Locate every blood parasite and identify its species.
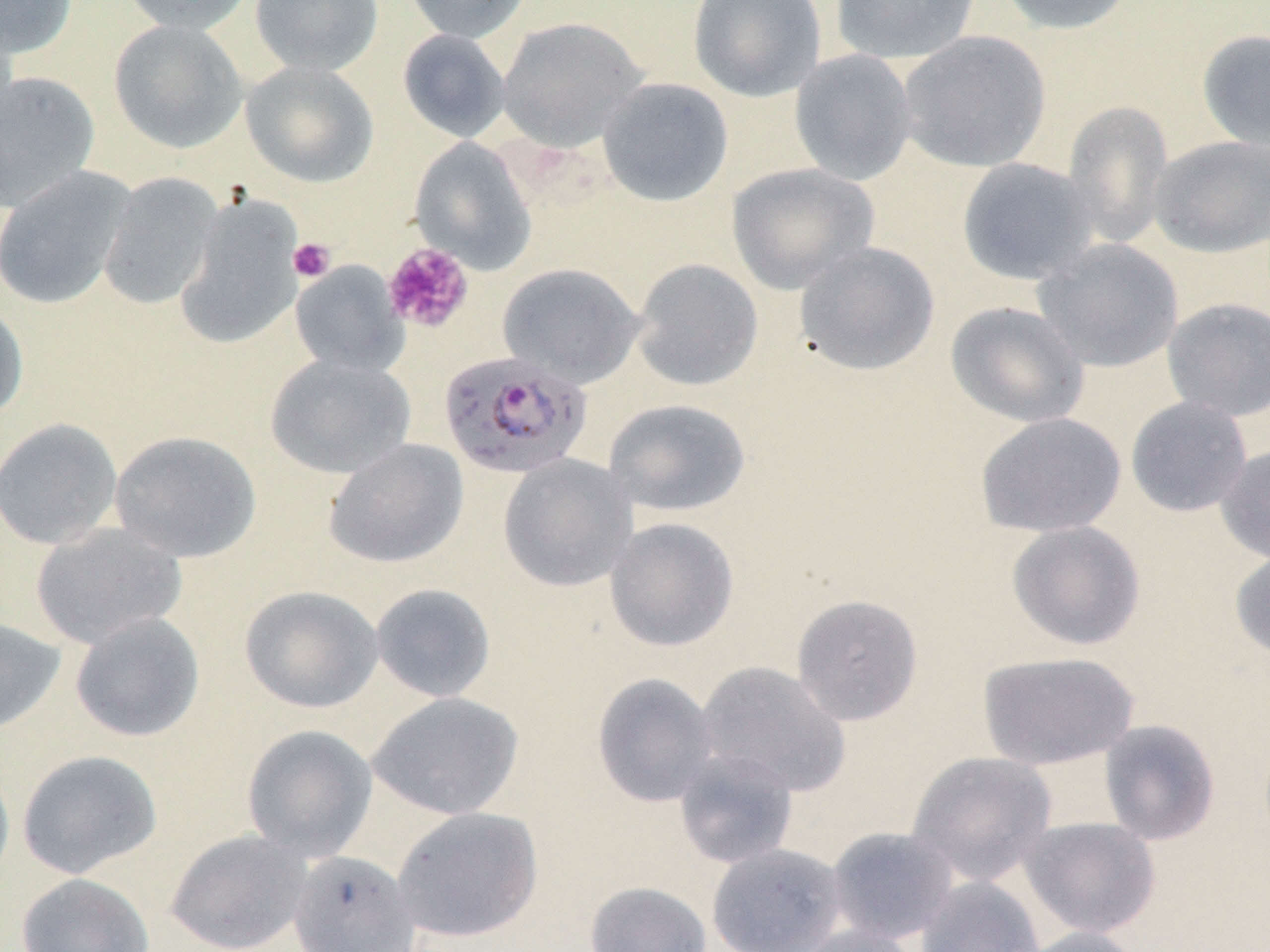

Approximate bounding boxes as named x1/y1/x2/y2 corners in pixels.
Plasmodium falciparum-infected red blood cells: (x1=438, y1=350, x2=592, y2=479).
No Plasmodium ovale, Plasmodium malariae, Plasmodium vivax, Babesia divergens, or Trypanosoma brucei observed.

slide-level diagnosis = Plasmodium falciparum
image size = 1270×952 pixels
field of view = one of a larger specimen
platelet locations = approximate bounding boxes as named x1/y1/x2/y2 corners in pixels: (x1=287, y1=238, x2=335, y2=283), (x1=381, y1=242, x2=474, y2=333)
preparation = thin blood film
modality = light microscopy
stain = May-Grünwald-Giemsa
uninfected red blood cell locations = approximate bounding boxes as named x1/y1/x2/y2 corners in pixels: (x1=0, y1=0, x2=78, y2=59), (x1=120, y1=0, x2=257, y2=34), (x1=249, y1=0, x2=383, y2=77), (x1=401, y1=0, x2=533, y2=44), (x1=687, y1=0, x2=827, y2=102), (x1=829, y1=0, x2=981, y2=66), (x1=994, y1=0, x2=1138, y2=36), (x1=497, y1=16, x2=649, y2=152), (x1=109, y1=18, x2=248, y2=153), (x1=1196, y1=28, x2=1270, y2=153), (x1=397, y1=29, x2=511, y2=142), (x1=897, y1=30, x2=1051, y2=173), (x1=789, y1=48, x2=917, y2=186), (x1=241, y1=60, x2=379, y2=188), (x1=0, y1=70, x2=100, y2=211), (x1=597, y1=77, x2=734, y2=207), (x1=1062, y1=100, x2=1174, y2=249), (x1=1149, y1=135, x2=1270, y2=258), (x1=410, y1=137, x2=537, y2=274), (x1=956, y1=158, x2=1097, y2=285), (x1=726, y1=162, x2=880, y2=295), (x1=0, y1=166, x2=137, y2=309), (x1=98, y1=172, x2=222, y2=310), (x1=174, y1=196, x2=304, y2=349), (x1=1034, y1=238, x2=1183, y2=373), (x1=793, y1=241, x2=941, y2=377), (x1=630, y1=258, x2=763, y2=391), (x1=290, y1=261, x2=408, y2=377), (x1=497, y1=262, x2=644, y2=388), (x1=1161, y1=298, x2=1270, y2=422), (x1=0, y1=299, x2=29, y2=425), (x1=945, y1=300, x2=1090, y2=429), (x1=265, y1=353, x2=416, y2=479), (x1=1125, y1=395, x2=1253, y2=517), (x1=603, y1=398, x2=751, y2=517), (x1=975, y1=412, x2=1127, y2=538), (x1=0, y1=417, x2=123, y2=550), (x1=109, y1=430, x2=262, y2=563), (x1=323, y1=438, x2=469, y2=568), (x1=1216, y1=443, x2=1270, y2=564), (x1=497, y1=455, x2=638, y2=593), (x1=604, y1=517, x2=739, y2=651), (x1=1006, y1=520, x2=1146, y2=651), (x1=30, y1=522, x2=187, y2=649), (x1=1230, y1=548, x2=1270, y2=662), (x1=369, y1=583, x2=497, y2=702), (x1=239, y1=585, x2=384, y2=714), (x1=791, y1=594, x2=924, y2=727), (x1=69, y1=612, x2=205, y2=743), (x1=0, y1=616, x2=66, y2=736), (x1=976, y1=650, x2=1140, y2=770), (x1=695, y1=661, x2=851, y2=798), (x1=591, y1=672, x2=720, y2=808), (x1=367, y1=691, x2=525, y2=821), (x1=1097, y1=718, x2=1221, y2=846), (x1=240, y1=724, x2=378, y2=861), (x1=17, y1=749, x2=163, y2=879), (x1=673, y1=749, x2=800, y2=869), (x1=905, y1=751, x2=1058, y2=886), (x1=0, y1=757, x2=15, y2=891), (x1=391, y1=806, x2=544, y2=943), (x1=1018, y1=816, x2=1161, y2=938), (x1=825, y1=826, x2=960, y2=944), (x1=164, y1=829, x2=314, y2=952), (x1=706, y1=842, x2=848, y2=952), (x1=289, y1=850, x2=422, y2=951), (x1=16, y1=872, x2=155, y2=952), (x1=915, y1=876, x2=1045, y2=952), (x1=583, y1=881, x2=712, y2=952), (x1=790, y1=923, x2=922, y2=952), (x1=1017, y1=926, x2=1143, y2=952)
magnification = 1000x